Describe the morphology of the red blood cells.
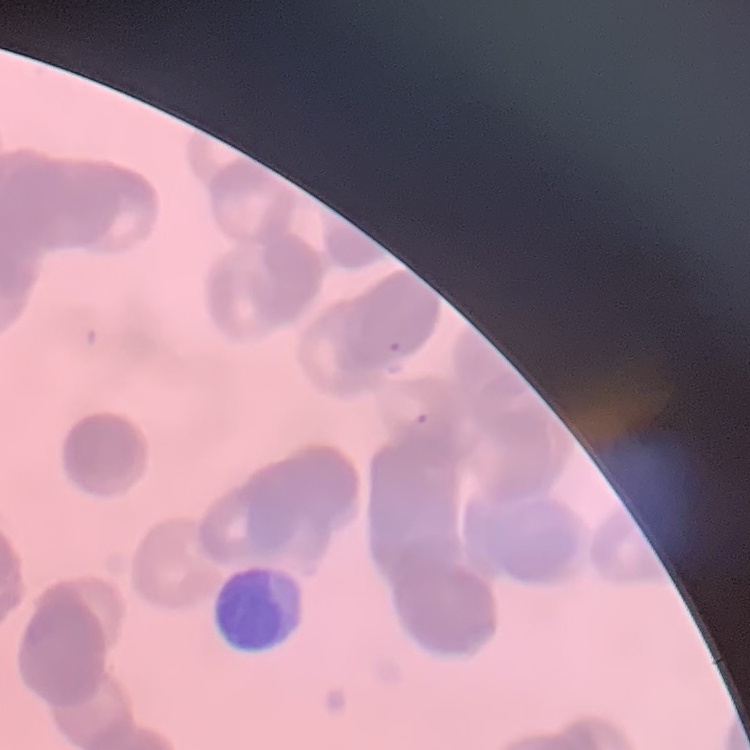

They show rouleaux formation.

stain = Field's or Giemsa
image type = one tile cut from a larger photomicrograph
preparation = thin blood smear